Identify the cell.
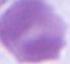

This is an erythrocyte.

{
  "magnification": "1000x",
  "modality": "micrograph"
}